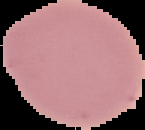

Malaria status: uninfected. Cell region segmented out of the field of view; the surrounding area is masked to black. From a thin blood film. Image is 145×130 pixels.